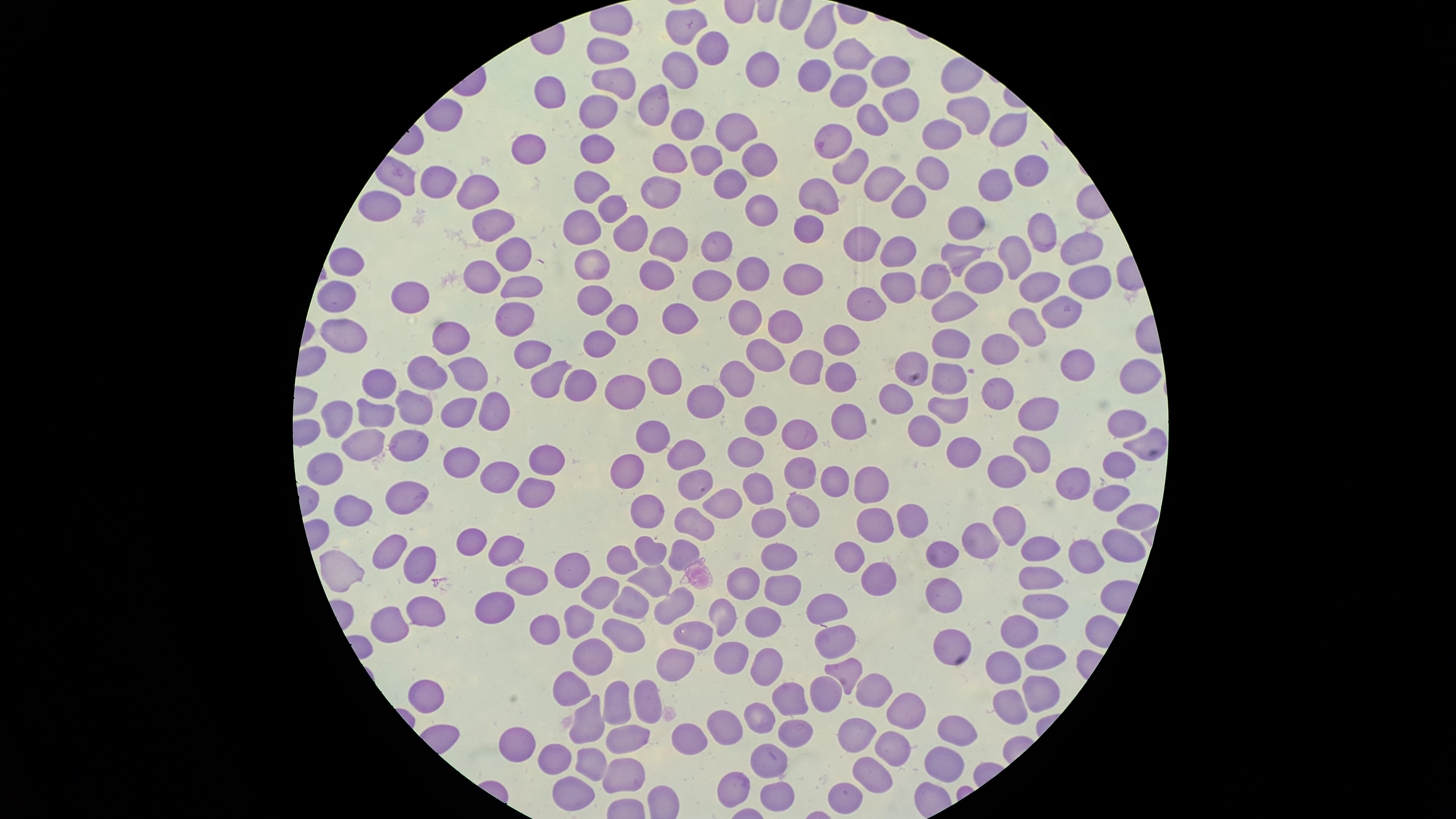
parasitized red blood cells = approximate marker points as (x, y) in pixels: (826, 144)
presence = malaria parasites seen
preparation = thin blood smear
uninfected red blood cells = approximate marker points as (x, y) in pixels: (686, 23), (818, 30), (709, 47), (606, 53), (855, 59), (679, 69), (762, 70), (890, 72), (815, 74), (614, 80), (844, 85), (547, 90), (659, 96), (895, 105), (596, 108), (965, 113), (864, 124), (1004, 124), (687, 125), (730, 131), (940, 137), (522, 139), (592, 145), (669, 155), (708, 158), (752, 163), (1024, 168), (850, 171), (930, 175), (877, 179), (434, 181), (585, 182), (726, 184), (663, 186), (995, 186), (476, 187), (821, 195), (913, 200), (377, 204), (609, 204), (756, 210), (494, 221), (583, 224), (968, 225), (810, 229), (1043, 233), (627, 236), (711, 241), (670, 242), (863, 244), (1081, 247), (903, 252), (960, 252), (1014, 252), (507, 254), (588, 262), (349, 266), (653, 269), (481, 272), (756, 277), (808, 279), (941, 280), (1092, 280), (714, 281), (981, 282), (525, 283), (897, 286), (1034, 286), (412, 296), (337, 297), (600, 299), (864, 300), (958, 302), (680, 312), (1059, 313), (511, 316), (621, 316), (742, 319), (789, 329), (1031, 332), (444, 335), (347, 337), (842, 338), (954, 341), (597, 343), (1000, 345), (534, 351), (760, 354), (912, 359), (1070, 362), (465, 363), (805, 363), (1136, 367), (427, 368), (577, 376), (953, 376), (377, 379), (662, 379), (736, 379), (837, 379), (545, 380), (996, 390), (625, 391), (705, 398), (896, 403), (409, 406), (451, 406), (486, 406), (946, 408), (376, 409), (339, 411), (848, 415), (1034, 415), (762, 420), (1125, 423), (922, 427), (651, 430), (796, 432), (1148, 442), (407, 446), (366, 447), (749, 448), (966, 448), (1036, 448), (684, 450), (544, 455), (460, 457), (627, 460), (1007, 463), (1124, 464), (330, 467), (798, 472), (495, 477), (831, 479), (1076, 479), (697, 481), (756, 485), (871, 487), (536, 489), (401, 495), (1108, 496), (723, 501), (798, 509), (354, 511), (646, 516), (1131, 517), (904, 519), (691, 521), (768, 521), (1011, 522), (875, 527), (985, 536), (470, 537), (1121, 542), (1044, 543), (380, 548), (507, 548), (646, 548), (676, 548), (947, 549), (409, 555), (776, 555), (848, 556), (1092, 556), (620, 561), (339, 565), (562, 572), (872, 575), (651, 576), (1040, 577), (519, 581), (740, 582), (778, 589), (946, 593), (594, 595), (625, 600), (493, 603), (667, 606), (1038, 606), (824, 608), (427, 615), (719, 615), (575, 621), (387, 622), (756, 624), (541, 631), (622, 631), (1014, 634), (832, 635), (688, 638), (954, 642), (728, 650), (599, 653), (1036, 654), (762, 658), (669, 665), (1002, 667), (840, 671), (574, 689), (823, 689), (870, 689), (1032, 695), (794, 696), (642, 698), (429, 699), (611, 704), (1004, 706), (904, 709), (758, 715), (593, 726), (958, 726), (793, 728), (722, 729), (856, 729), (513, 736), (622, 736), (683, 738), (891, 744), (763, 753), (942, 757), (550, 759), (589, 763), (871, 768), (628, 775), (732, 783), (571, 788), (769, 792), (842, 794)
stain = Giemsa
field of view = single
image size = 1456×819 pixels
species = Plasmodium falciparum
visible region = circular
capture = smartphone photograph through the microscope eyepiece